Classify this cell by malaria status.
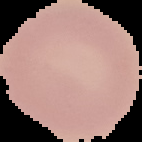

It is uninfected.

Summary:
  - Preparation: thin blood smear
  - Image type: cell region segmented out of the field of view; surrounding area masked to black
  - Image size: 142×142 pixels